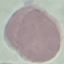
Summary:
  - Malaria status: uninfected
  - Stain: Giemsa
  - Capture: smartphone camera at the microscope eyepiece
  - Preparation: thin blood film
  - Image type: cell patch, automatically extracted from a larger field of view and resized to 64 × 64 pixels